Name the parasite shown.
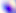

This is Toxoplasma gondii.

modality = micrograph
magnification = 400x